Report the malaria status of this cell.
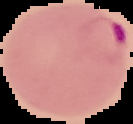

Parasitized.

preparation: thin blood film
image_size: 133×124 pixels
image_type: cell region segmented out of the field of view; surrounding area masked to black